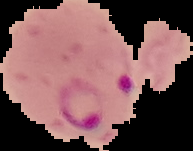

Summary:
  - Image size: 193×151 pixels
  - Malaria status: parasitized
  - Image type: segmented cell region with the area outside set to black
  - Preparation: thin blood smear